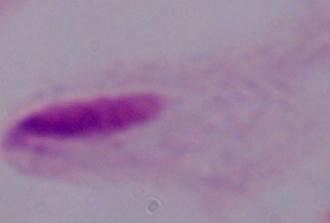
Captured at 1000x magnification. A trichomonad is shown. Photomicrograph.